Locate and identify every blood parasite.
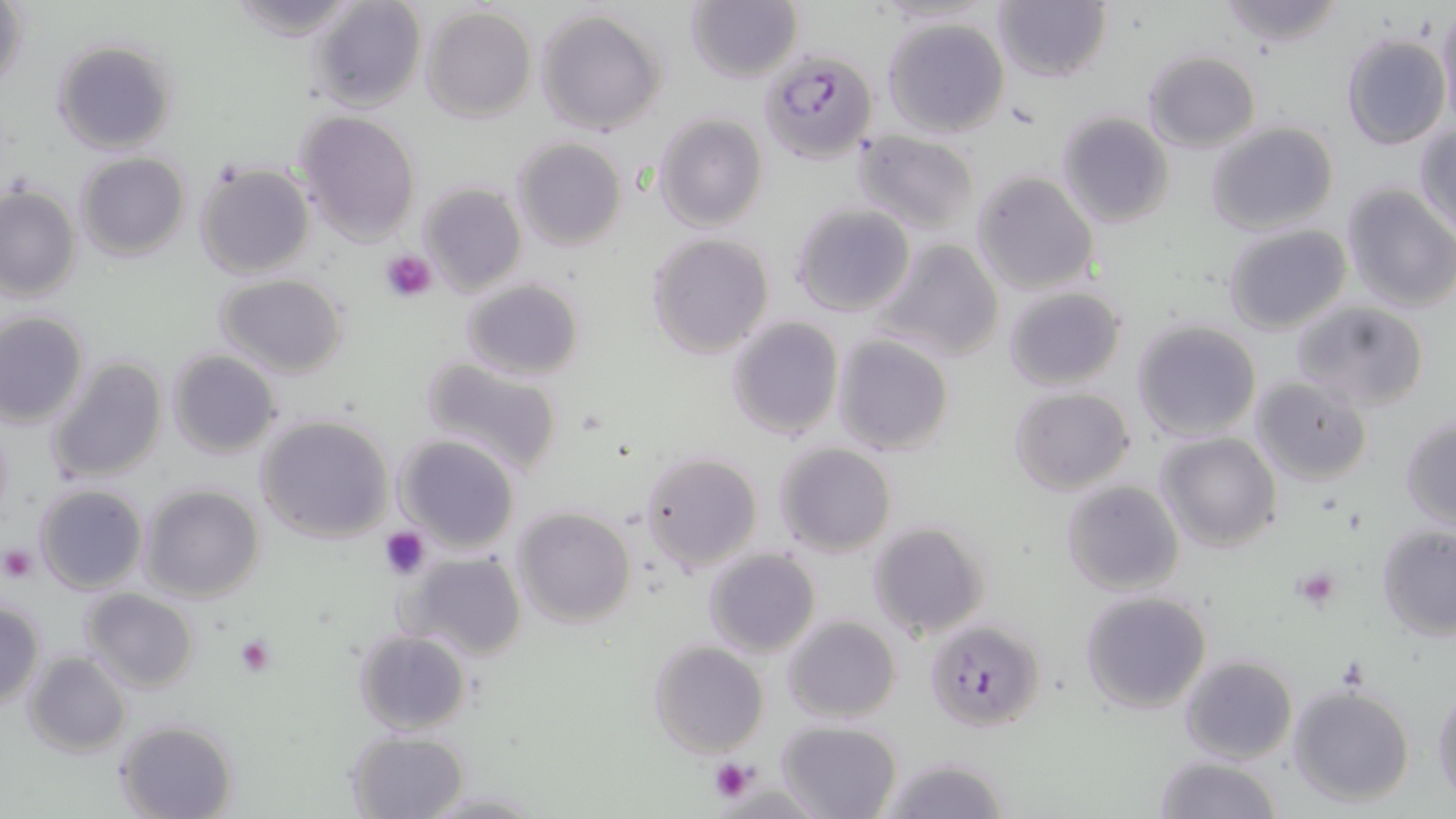

Approximate bounding boxes as [x1, y1, x2, y2] in pixels.
Plasmodium falciparum-infected red blood cells: [759, 51, 877, 164], [923, 618, 1045, 732].
No Plasmodium ovale, Plasmodium malariae, Plasmodium vivax, Babesia divergens, or Trypanosoma brucei observed.

slide_level_diagnosis: Plasmodium falciparum
field_of_view: single
stain: May-Grünwald-Giemsa
image_size: 1456×819 pixels
modality: light microscopy
magnification: 1000x
preparation: thin blood film
platelet_locations: 'approximate bounding boxes as [x1, y1, x2, y2] in pixels: [381, 248, 438, 302], [380, 525, 429, 578], [1, 545, 39, 582], [1293, 566, 1340, 610], [233, 634, 275, 676], [709, 757, 756, 802]'
uninfected_red_blood_cell_locations: 'approximate bounding boxes as [x1, y1, x2, y2] in pixels: [223, 0, 368, 43], [308, 0, 428, 113], [991, 0, 1112, 84], [1217, 0, 1349, 49], [1, 1, 29, 100], [684, 1, 803, 84], [1436, 4, 1456, 126], [421, 7, 536, 123], [535, 8, 666, 135], [881, 15, 1011, 138], [1341, 33, 1450, 150], [50, 37, 180, 156], [1143, 51, 1261, 153], [293, 110, 422, 245], [1055, 111, 1174, 228], [652, 112, 769, 232], [1207, 122, 1338, 235], [1415, 123, 1456, 236], [853, 130, 982, 236], [510, 136, 627, 251], [75, 153, 189, 261], [193, 162, 315, 280], [972, 171, 1099, 296], [419, 182, 527, 298], [0, 184, 80, 302], [1341, 185, 1455, 312], [789, 202, 916, 317], [1223, 224, 1350, 335], [646, 231, 775, 359], [872, 236, 1006, 363], [215, 272, 350, 379], [461, 278, 584, 380], [1003, 284, 1127, 390], [1292, 301, 1426, 413], [0, 311, 89, 428], [726, 316, 845, 440], [1131, 320, 1262, 442], [831, 335, 956, 456], [167, 350, 281, 458], [47, 355, 169, 484], [418, 355, 565, 477], [1250, 376, 1372, 486], [1008, 387, 1135, 495], [254, 414, 395, 544], [1400, 416, 1456, 529], [1156, 432, 1281, 553], [394, 435, 522, 553], [772, 442, 898, 557], [640, 450, 762, 573], [1061, 480, 1184, 597], [34, 483, 148, 594], [139, 484, 266, 603], [513, 506, 636, 628], [868, 521, 990, 640], [1376, 523, 1456, 640], [702, 548, 820, 659], [399, 551, 527, 660], [79, 588, 198, 692], [1079, 590, 1211, 714], [1, 601, 45, 707], [783, 615, 901, 723], [353, 628, 472, 735], [649, 641, 768, 757], [24, 652, 130, 757], [1179, 655, 1299, 766], [1287, 683, 1416, 808], [1431, 684, 1455, 806], [775, 719, 903, 819], [113, 720, 237, 819], [346, 730, 471, 819], [1154, 754, 1281, 819], [877, 755, 1011, 819], [415, 785, 547, 817]'